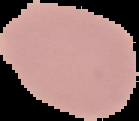 From a thin blood film. Result: no Plasmodium parasites detected. Cell region segmented out of the field of view; the surrounding area is masked to black. Image is 139×121 pixels.